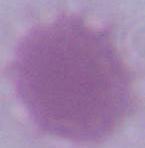

modality = micrograph
identification = erythrocyte
magnification = 1000x